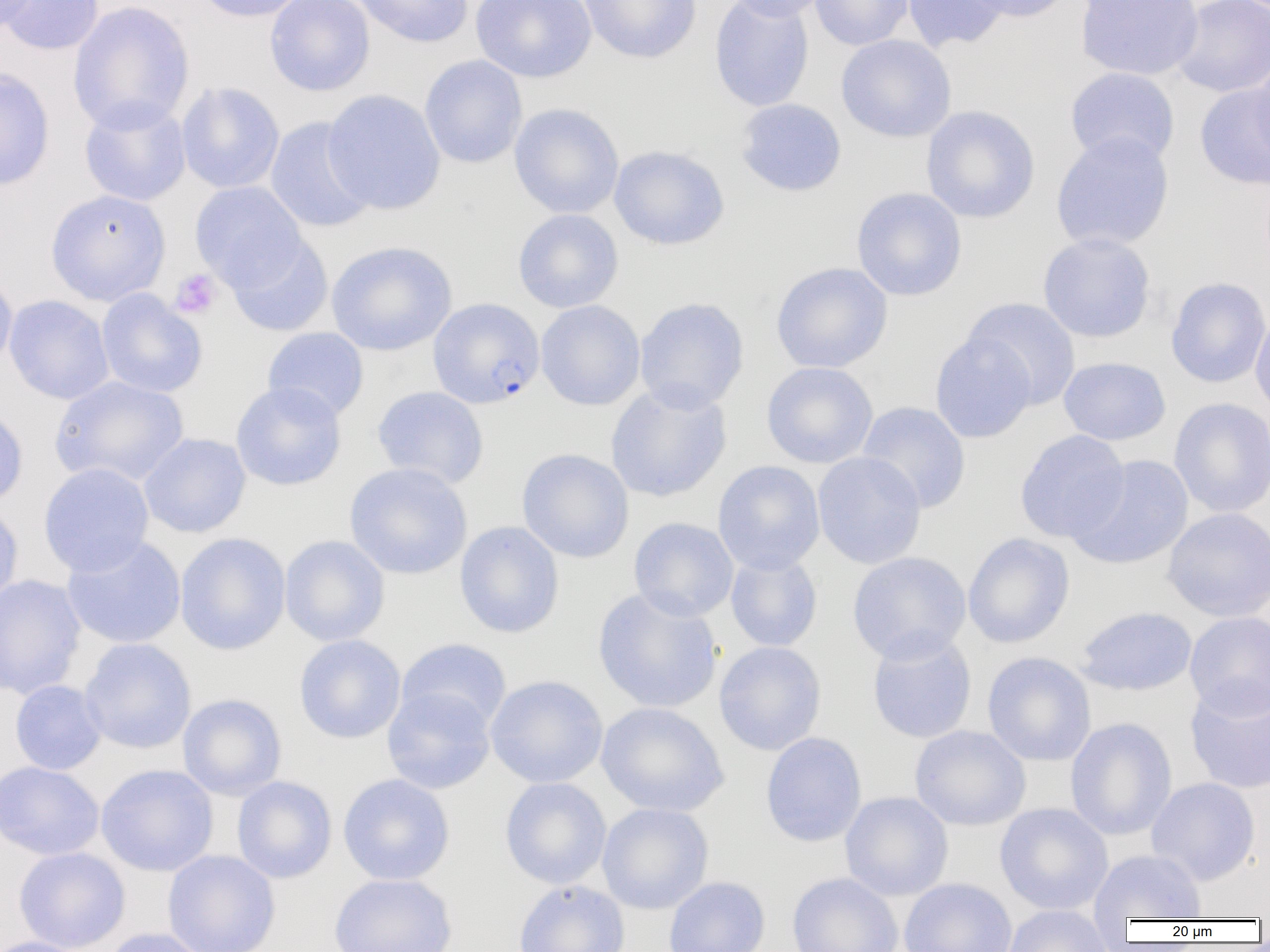

slide-level diagnosis = Plasmodium falciparum
magnification = 1000x
platelet locations = approximate bounding boxes as [x1, y1, x2, y2] in pixels: [169, 269, 222, 319]
uninfected red blood cell locations = approximate bounding boxes as [x1, y1, x2, y2] in pixels: [0, 0, 37, 34], [1, 0, 104, 56], [193, 0, 310, 22], [265, 0, 375, 96], [350, 0, 474, 48], [471, 0, 597, 83], [578, 0, 702, 64], [709, 0, 814, 112], [721, 0, 833, 21], [809, 0, 914, 50], [902, 0, 1010, 52], [960, 0, 1073, 23], [1076, 0, 1204, 81], [1171, 0, 1269, 98], [68, 1, 195, 134], [835, 34, 956, 142], [419, 55, 528, 168], [1249, 56, 1270, 165], [0, 67, 55, 191], [1065, 67, 1180, 168], [176, 81, 285, 194], [1194, 83, 1270, 191], [322, 89, 446, 215], [79, 97, 191, 207], [735, 98, 847, 197], [509, 102, 624, 219], [921, 106, 1041, 224], [264, 116, 377, 234], [1050, 131, 1175, 252], [608, 145, 730, 250], [190, 182, 307, 290], [851, 187, 968, 301], [45, 188, 170, 306], [512, 209, 624, 313], [225, 232, 333, 337], [1037, 232, 1156, 343], [326, 240, 457, 356], [771, 262, 893, 373], [0, 270, 18, 376], [1166, 276, 1270, 388], [96, 289, 208, 398], [4, 295, 114, 405], [634, 297, 750, 413], [961, 297, 1082, 410], [536, 300, 646, 411], [1249, 308, 1270, 419], [262, 327, 369, 422], [930, 332, 1036, 444], [1058, 356, 1171, 446], [761, 361, 879, 468], [50, 375, 189, 488], [230, 381, 347, 491], [605, 381, 732, 503], [371, 386, 490, 490], [1168, 397, 1270, 518], [857, 401, 971, 514], [0, 403, 28, 509], [1014, 430, 1130, 543], [138, 433, 251, 538], [516, 448, 634, 563], [812, 452, 927, 569], [1069, 454, 1194, 570], [713, 460, 825, 574], [343, 462, 473, 580], [38, 463, 155, 577], [0, 502, 24, 612], [1162, 506, 1270, 622], [629, 517, 739, 622], [454, 521, 565, 639], [174, 532, 292, 655], [962, 533, 1075, 648], [61, 535, 186, 649], [279, 535, 390, 646], [725, 551, 823, 652], [847, 551, 972, 664], [0, 574, 87, 700], [592, 587, 723, 714], [1074, 606, 1198, 697], [1185, 611, 1270, 717], [866, 630, 977, 744], [294, 634, 406, 744], [79, 638, 196, 754], [396, 638, 512, 733], [714, 641, 826, 755], [982, 651, 1096, 766], [485, 674, 608, 788], [9, 680, 107, 775], [1184, 681, 1270, 794], [382, 687, 496, 794], [177, 693, 287, 800], [595, 702, 728, 817], [1065, 717, 1177, 841], [909, 725, 1031, 831], [760, 732, 867, 847], [0, 761, 104, 860], [96, 763, 218, 876], [337, 773, 455, 885], [232, 775, 337, 883], [500, 777, 612, 889], [1146, 777, 1261, 886], [840, 791, 953, 900], [596, 802, 714, 914], [994, 802, 1114, 915], [13, 846, 131, 952], [162, 849, 280, 952], [1089, 849, 1206, 921], [787, 872, 904, 952], [328, 873, 458, 952], [663, 876, 770, 952], [899, 878, 1017, 952], [512, 879, 630, 952], [1002, 905, 1114, 952], [101, 927, 215, 952], [0, 935, 95, 952]
image size = 1270×952 pixels
modality = light microscopy
Plasmodium falciparum-infected red blood cell locations = approximate bounding boxes as [x1, y1, x2, y2] in pixels: [428, 298, 545, 409]
preparation = thin blood film
field of view = single